Assess this cell for malaria.
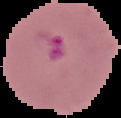

It is parasitized.

Summary:
  - Image type: segmented cell region on a black background
  - Preparation: thin blood film
  - Image size: 121×118 pixels